Assess the morphology of the red blood cells.
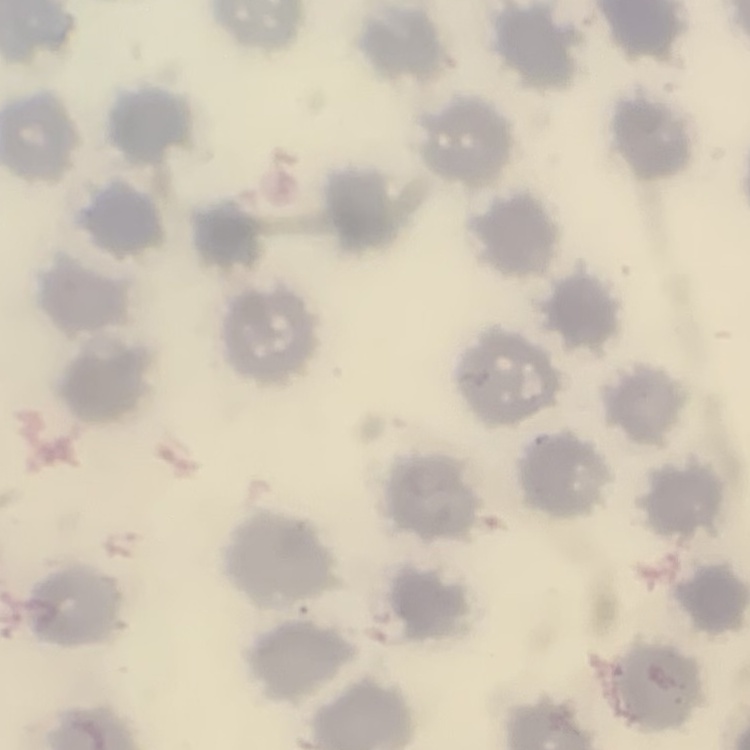

No rouleaux formation.

Summary:
  - Stain: Field's or Giemsa
  - Preparation: thin blood smear
  - Image type: one tile cut from a larger photomicrograph